State which parasite is depicted.
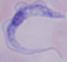

This is a trypanosome.

Summary:
  - Modality: micrograph
  - Magnification: 1000x